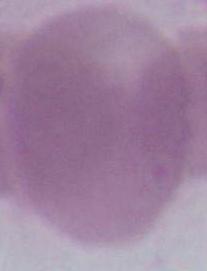

Summary:
  - Modality: photomicrograph
  - Identification: erythrocyte
  - Magnification: 1000x